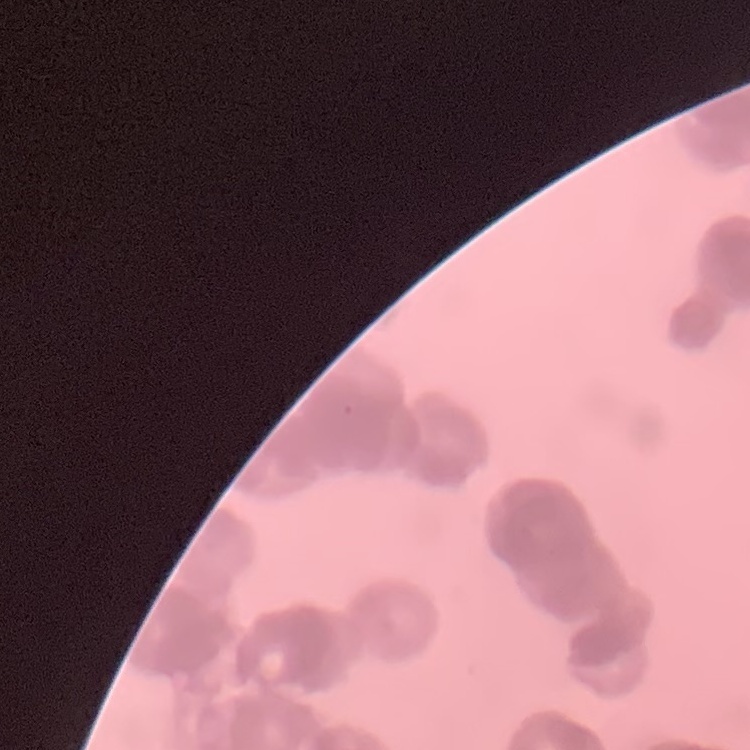
erythrocyte morphology = rouleaux formation
image type = square crop of a larger photomicrograph
preparation = thin peripheral smear
stain = Field's or Giemsa